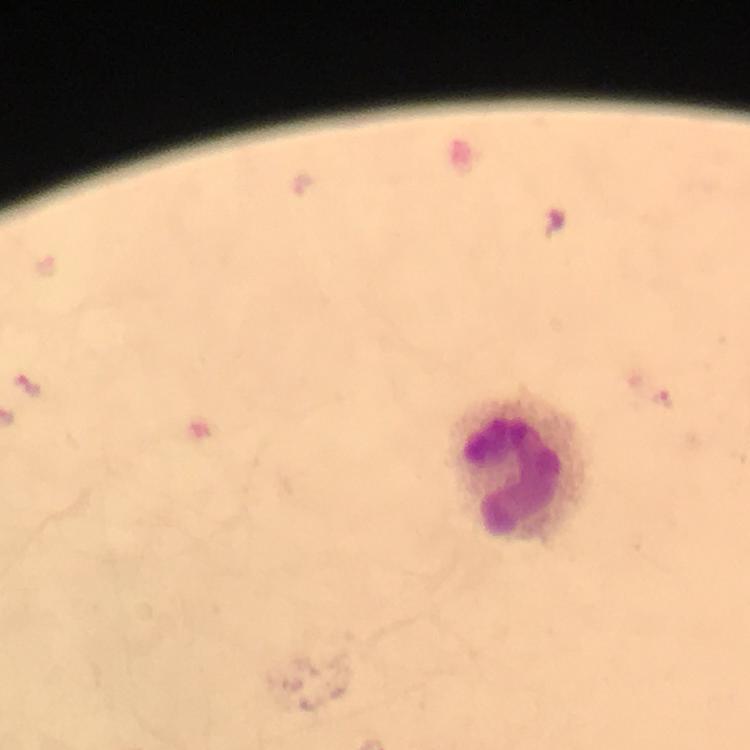

Approximate centers as {x, y} in pixels.
Summary:
  - Malaria parasite locations: {29, 387}, {661, 399}
  - Leukocyte locations: {518, 471}
  - Context: from a diagnostic examination for malaria
  - Magnification: 100x
  - Stain: Giemsa
  - Cropped from: one field of view
  - Capture: smartphone camera through the microscope
  - Preparation: thick smear
  - Immersion oil: applied
  - Image size: 750×750 pixels